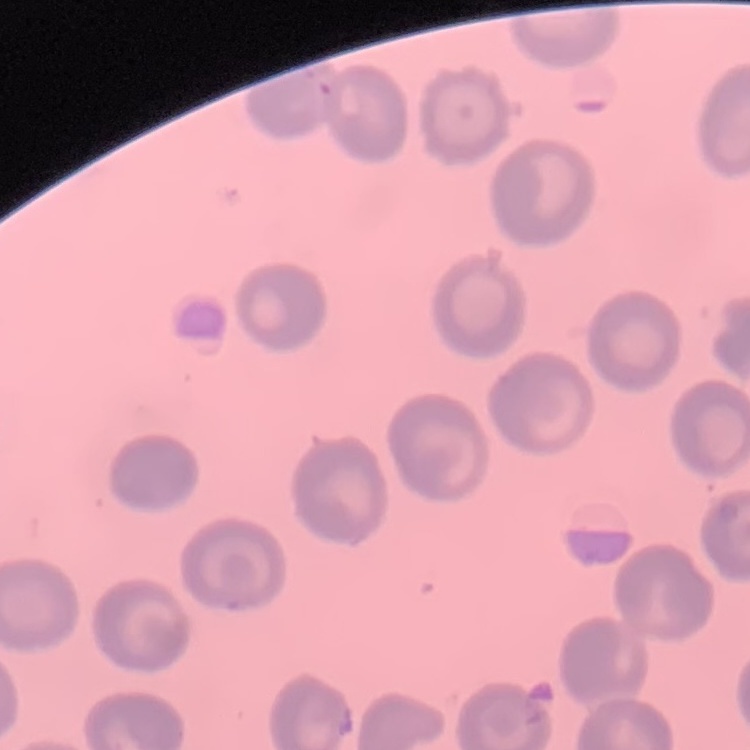
Summary:
  - Erythrocyte morphology: no rouleaux formation
  - Preparation: thin peripheral smear
  - Image type: square crop of a larger photomicrograph
  - Stain: Field's or Giemsa